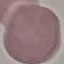
Result: no malaria parasites seen. Automatically extracted cell patch, resized to 64 × 64 pixels. Giemsa-stained preparation. Photographed with a smartphone camera at the microscope eyepiece. Thin smear of blood.